Outline each Plasmodium ovale-infected red blood cell.
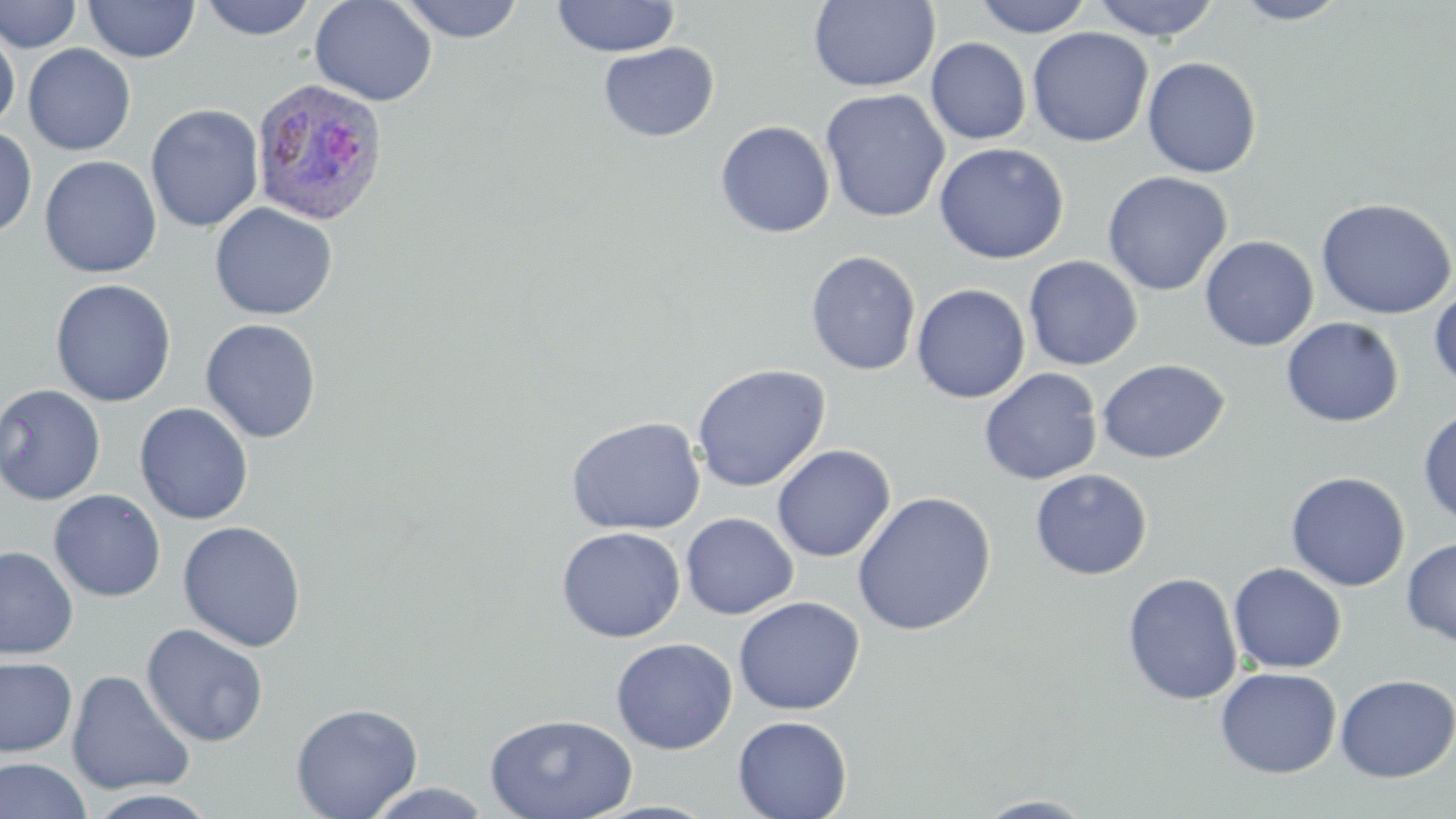
Approximate bounding boxes as named x1/y1/x2/y2 corners in pixels.
Plasmodium ovale-infected red blood cells: (x1=250, y1=76, x2=390, y2=226).

Summary:
  - Uninfected red blood cell locations: (x1=1, y1=0, x2=83, y2=53), (x1=197, y1=0, x2=318, y2=41), (x1=309, y1=0, x2=437, y2=106), (x1=397, y1=0, x2=525, y2=43), (x1=551, y1=0, x2=680, y2=58), (x1=972, y1=0, x2=1094, y2=38), (x1=1089, y1=0, x2=1222, y2=41), (x1=1230, y1=0, x2=1352, y2=25), (x1=84, y1=1, x2=200, y2=63), (x1=808, y1=1, x2=940, y2=92), (x1=0, y1=23, x2=20, y2=132), (x1=1027, y1=26, x2=1153, y2=147), (x1=926, y1=37, x2=1031, y2=145), (x1=599, y1=42, x2=719, y2=142), (x1=23, y1=44, x2=136, y2=156), (x1=1142, y1=57, x2=1262, y2=179), (x1=820, y1=88, x2=950, y2=223), (x1=145, y1=104, x2=264, y2=233), (x1=715, y1=120, x2=835, y2=239), (x1=0, y1=126, x2=37, y2=240), (x1=933, y1=142, x2=1069, y2=264), (x1=39, y1=155, x2=161, y2=278), (x1=1102, y1=170, x2=1232, y2=296), (x1=1315, y1=197, x2=1456, y2=320), (x1=209, y1=202, x2=338, y2=321), (x1=1200, y1=235, x2=1319, y2=352), (x1=805, y1=250, x2=921, y2=376), (x1=1023, y1=255, x2=1143, y2=371), (x1=50, y1=278, x2=177, y2=407), (x1=911, y1=284, x2=1030, y2=404), (x1=1429, y1=287, x2=1456, y2=393), (x1=1281, y1=317, x2=1404, y2=427), (x1=200, y1=318, x2=322, y2=444), (x1=1096, y1=359, x2=1229, y2=464), (x1=692, y1=364, x2=830, y2=492), (x1=979, y1=368, x2=1102, y2=486), (x1=0, y1=383, x2=105, y2=505), (x1=134, y1=403, x2=254, y2=525), (x1=1418, y1=408, x2=1456, y2=529), (x1=565, y1=417, x2=706, y2=536), (x1=771, y1=443, x2=896, y2=562), (x1=1030, y1=469, x2=1152, y2=580), (x1=1285, y1=471, x2=1410, y2=591), (x1=48, y1=489, x2=166, y2=601), (x1=853, y1=491, x2=996, y2=636), (x1=681, y1=512, x2=798, y2=619), (x1=177, y1=520, x2=307, y2=652), (x1=556, y1=526, x2=685, y2=643), (x1=1401, y1=536, x2=1456, y2=647), (x1=0, y1=546, x2=78, y2=659), (x1=1228, y1=562, x2=1347, y2=673), (x1=1122, y1=572, x2=1243, y2=705), (x1=733, y1=596, x2=865, y2=716), (x1=141, y1=623, x2=269, y2=747), (x1=611, y1=637, x2=737, y2=754), (x1=0, y1=656, x2=78, y2=758), (x1=1214, y1=666, x2=1341, y2=779), (x1=66, y1=670, x2=195, y2=796), (x1=1334, y1=674, x2=1456, y2=782), (x1=290, y1=701, x2=424, y2=819), (x1=484, y1=713, x2=638, y2=819), (x1=733, y1=715, x2=853, y2=819), (x1=0, y1=758, x2=93, y2=818), (x1=364, y1=782, x2=495, y2=817), (x1=86, y1=788, x2=223, y2=817), (x1=974, y1=794, x2=1099, y2=818)
  - Slide-level diagnosis: Plasmodium ovale
  - Magnification: 1000x
  - Preparation: thin blood smear
  - Image size: 1456×819 pixels
  - Modality: optical microscopy
  - Field of view: single
  - Stain: May-Grünwald-Giemsa